State which parasite is depicted.
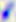

This is Toxoplasma gondii.

Summary:
  - Magnification: 400x
  - Modality: photomicrograph